Name the blood parasite species.
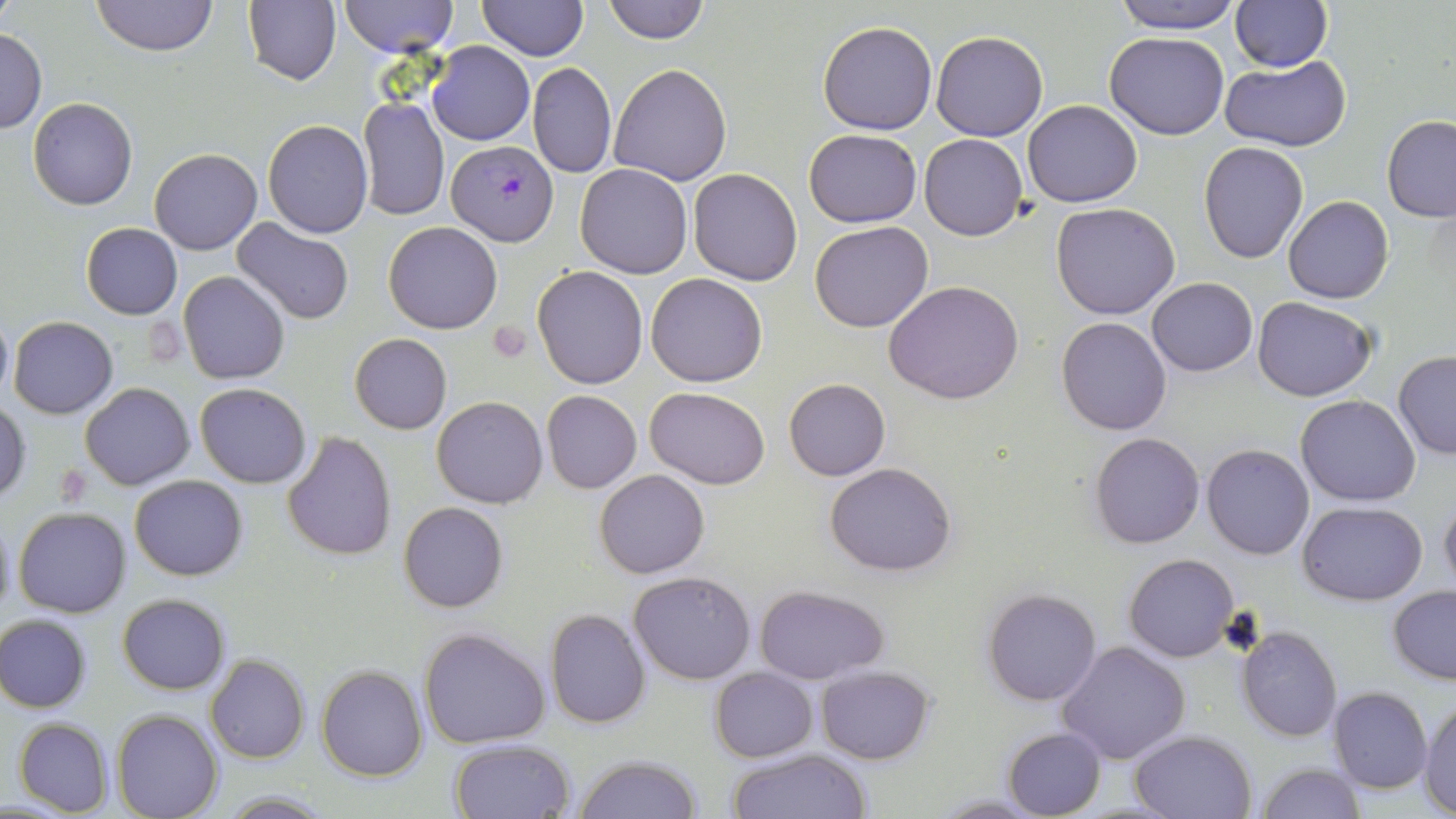
Plasmodium falciparum.

Summary:
  - Coordinate format: approximate bounding boxes as (x1,y1)-(x2,y2) corner pairs in pixels
  - Uninfected red blood cell locations: (91,0)-(218,56), (244,0)-(342,87), (340,0)-(456,56), (476,0)-(589,60), (604,0)-(709,44), (1110,0)-(1243,35), (1229,0)-(1332,72), (818,21)-(938,135), (0,28)-(46,133), (932,31)-(1049,141), (1105,31)-(1230,140), (429,41)-(534,145), (1221,57)-(1351,153), (529,63)-(616,177), (610,63)-(731,185), (359,96)-(449,221), (28,98)-(138,210), (1022,100)-(1143,206), (1382,115)-(1456,221), (263,119)-(374,237), (805,129)-(922,227), (919,133)-(1028,241), (1199,142)-(1307,263), (149,148)-(262,255), (576,164)-(692,279), (688,169)-(802,285), (1284,196)-(1394,304), (1051,202)-(1180,320), (230,218)-(357,327), (809,221)-(933,333), (80,222)-(183,319), (383,222)-(503,333), (533,266)-(648,390), (179,272)-(289,384), (648,274)-(766,386), (1147,278)-(1257,376), (885,280)-(1026,405), (1252,296)-(1378,402), (0,309)-(12,403), (1057,317)-(1171,435), (8,318)-(117,419), (350,333)-(452,434), (1394,353)-(1456,460), (784,378)-(889,480), (80,383)-(195,490), (195,383)-(312,487), (646,387)-(769,490), (541,391)-(641,493), (431,395)-(549,508), (1296,395)-(1420,507), (0,401)-(30,505), (281,432)-(397,558), (1089,432)-(1206,549), (1202,444)-(1314,560), (825,462)-(956,575), (594,468)-(710,579), (129,474)-(248,581), (1439,493)-(1456,594), (1298,500)-(1426,603), (399,501)-(508,612), (14,507)-(130,618), (0,514)-(15,622), (1123,553)-(1240,662), (629,572)-(755,684), (756,584)-(889,684), (1388,584)-(1456,684), (982,587)-(1102,706), (117,593)-(231,694), (545,609)-(650,728), (0,614)-(90,713), (419,626)-(550,749), (1236,627)-(1342,742), (1057,640)-(1190,766), (206,654)-(309,764), (316,665)-(427,781), (816,666)-(934,764), (709,667)-(818,762), (1328,687)-(1433,793), (1419,700)-(1455,816), (112,711)-(223,819), (13,718)-(115,816), (1002,726)-(1106,818), (1129,729)-(1257,818), (447,738)-(577,819), (726,748)-(870,819), (573,754)-(702,819), (1256,761)-(1365,819), (216,791)-(333,817), (932,793)-(1047,818)
  - Plasmodium falciparum-infected red blood cell locations: (445,140)-(560,246)
  - Platelet locations: (143,320)-(182,364), (486,320)-(532,361), (51,469)-(87,513)
  - Preparation: thin blood film
  - Stain: May-Grünwald-Giemsa
  - Field of view: single
  - Magnification: 1000x
  - Modality: light microscopy
  - Image size: 1456×819 pixels